Locate every Plasmodium vivax-infected red blood cell.
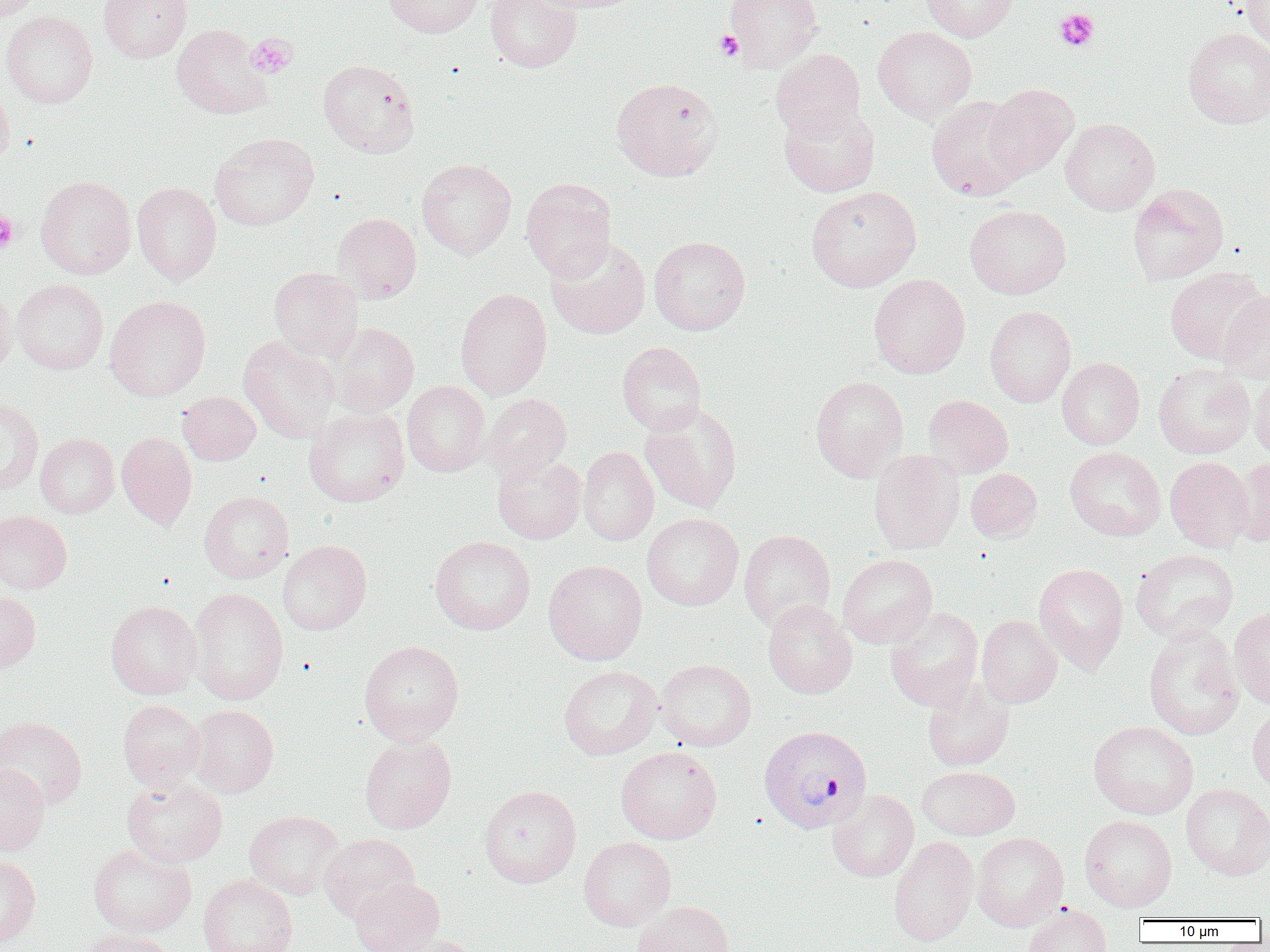

Approximate bounding boxes as [x1, y1, x2, y2] in pixels.
Plasmodium vivax-infected red blood cells: [758, 724, 872, 833].

Summary:
  - Uninfected red blood cell locations: [0, 0, 42, 20], [98, 0, 192, 63], [382, 0, 483, 38], [485, 0, 582, 72], [528, 0, 643, 13], [724, 0, 822, 71], [921, 0, 1018, 42], [1239, 0, 1269, 54], [1, 11, 98, 108], [172, 24, 274, 119], [872, 25, 977, 122], [1183, 27, 1270, 127], [770, 49, 865, 140], [318, 59, 420, 157], [611, 77, 723, 181], [0, 81, 15, 166], [984, 84, 1078, 180], [926, 95, 1030, 201], [779, 103, 880, 198], [1060, 118, 1160, 215], [209, 133, 319, 231], [417, 158, 517, 259], [35, 175, 136, 280], [521, 178, 617, 282], [132, 181, 222, 285], [1127, 183, 1229, 286], [806, 186, 921, 292], [965, 204, 1071, 299], [333, 212, 422, 303], [649, 235, 750, 335], [546, 237, 650, 339], [1165, 266, 1268, 364], [268, 267, 363, 362], [868, 273, 970, 378], [12, 278, 108, 374], [0, 281, 17, 378], [455, 288, 552, 400], [1218, 291, 1270, 382], [105, 295, 211, 401], [985, 305, 1076, 407], [329, 323, 419, 417], [238, 335, 340, 444], [617, 342, 706, 436], [1057, 357, 1145, 449], [1153, 363, 1255, 459], [1249, 370, 1270, 465], [810, 375, 909, 481], [402, 380, 490, 477], [177, 391, 261, 466], [482, 393, 571, 482], [923, 395, 1014, 478], [0, 397, 43, 493], [640, 402, 741, 513], [304, 407, 409, 507], [116, 431, 197, 529], [35, 433, 119, 518], [578, 446, 659, 546], [1065, 447, 1166, 541], [868, 449, 965, 555], [492, 452, 586, 544], [1165, 456, 1254, 552], [1231, 456, 1270, 546], [966, 468, 1042, 542], [199, 491, 294, 583], [0, 509, 72, 593], [642, 512, 744, 611], [739, 529, 836, 631], [430, 536, 536, 635], [278, 539, 372, 635], [1130, 548, 1239, 642], [838, 554, 937, 648], [543, 559, 647, 665], [1033, 562, 1129, 673], [188, 587, 288, 705], [0, 590, 41, 674], [105, 600, 203, 699], [763, 600, 857, 699], [1229, 606, 1270, 708], [885, 607, 983, 711], [976, 615, 1062, 708], [1143, 624, 1244, 741], [359, 640, 463, 745], [656, 658, 756, 751], [559, 665, 662, 760], [922, 678, 1015, 771], [118, 699, 205, 791], [1247, 703, 1270, 796], [188, 704, 279, 797], [0, 716, 87, 809], [1088, 720, 1199, 819], [359, 734, 457, 834], [616, 745, 722, 844], [0, 763, 50, 857], [917, 766, 1020, 840], [121, 777, 227, 867], [1181, 783, 1270, 880], [479, 785, 582, 888], [827, 790, 919, 882], [245, 810, 343, 899], [1079, 815, 1177, 911], [972, 832, 1069, 931], [319, 833, 420, 922], [579, 836, 676, 931], [889, 836, 979, 947], [88, 844, 196, 936], [0, 853, 41, 948], [198, 874, 297, 952], [350, 877, 444, 952], [633, 901, 735, 952], [1023, 905, 1112, 952], [79, 927, 175, 952], [380, 934, 484, 952]
  - Platelet locations: [1054, 9, 1100, 52], [715, 30, 743, 60], [246, 33, 297, 79], [0, 212, 18, 253]
  - Slide-level diagnosis: Plasmodium vivax
  - Modality: optical microscopy
  - Image size: 1270×952 pixels
  - Preparation: thin blood smear
  - Field of view: one of a larger specimen
  - Magnification: 1000x